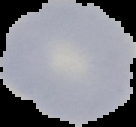

Cell region segmented out of the field of view; the surrounding area is masked to black. Result: negative for Plasmodium parasites. Image is 136×127 pixels. From a thin blood smear.